Name the parasite shown.
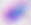

This is Toxoplasma gondii.

Summary:
  - Modality: photomicrograph
  - Magnification: 400x